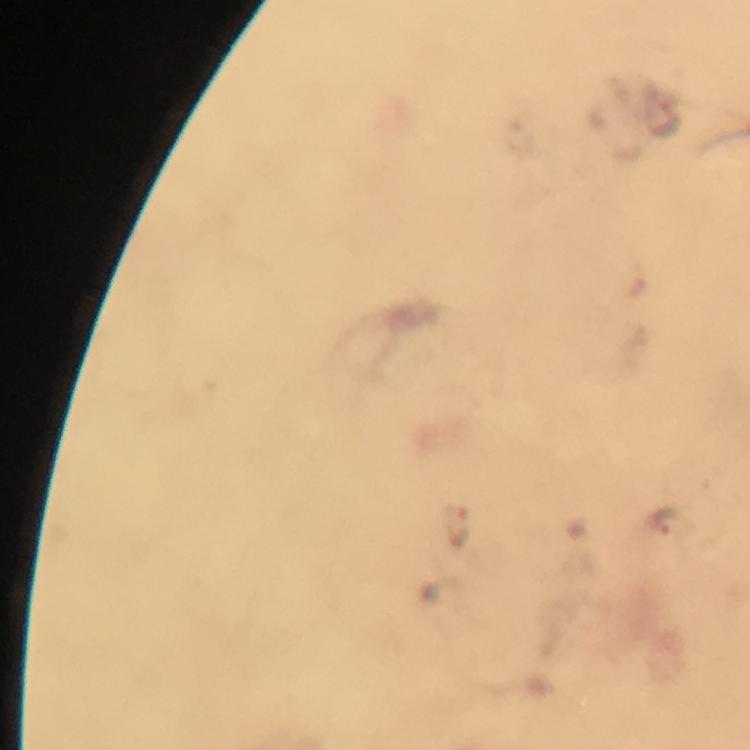
magnification = 100x
image size = 750×750 pixels
preparation = thick smear
context = from a diagnostic examination for malaria
capture = smartphone camera through the microscope
cropped from = one field of view
stain = Giemsa
immersion oil = applied
malaria parasite locations = approximate centers as [x, y] in pixels: [666, 121], [662, 521], [458, 528]